Describe the morphology of the red blood cells.
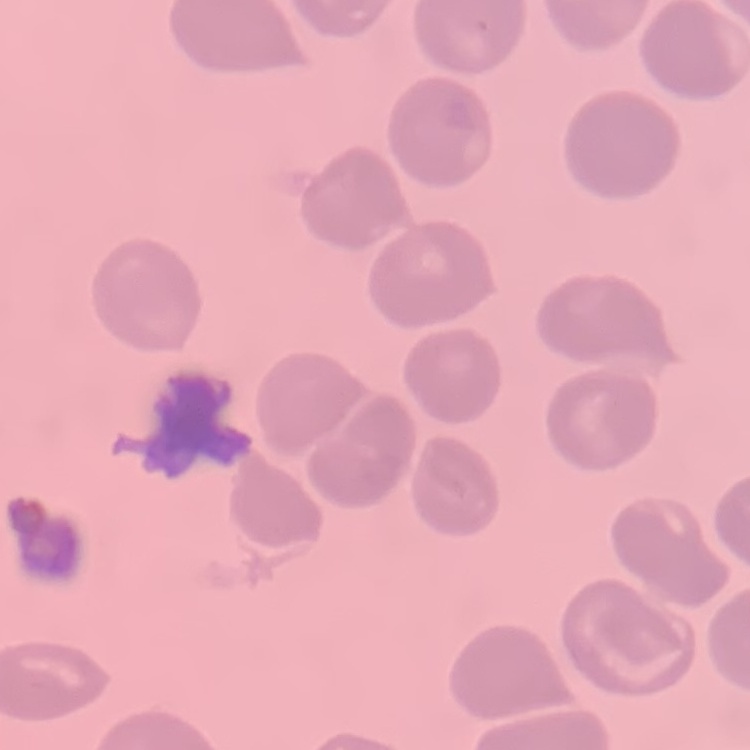
They show no rouleaux formation.

{
  "preparation": "thin peripheral smear",
  "stain": "Field's or Giemsa",
  "image_type": "square crop of a larger photomicrograph"
}